Locate every Plasmodium falciparum-infected red blood cell.
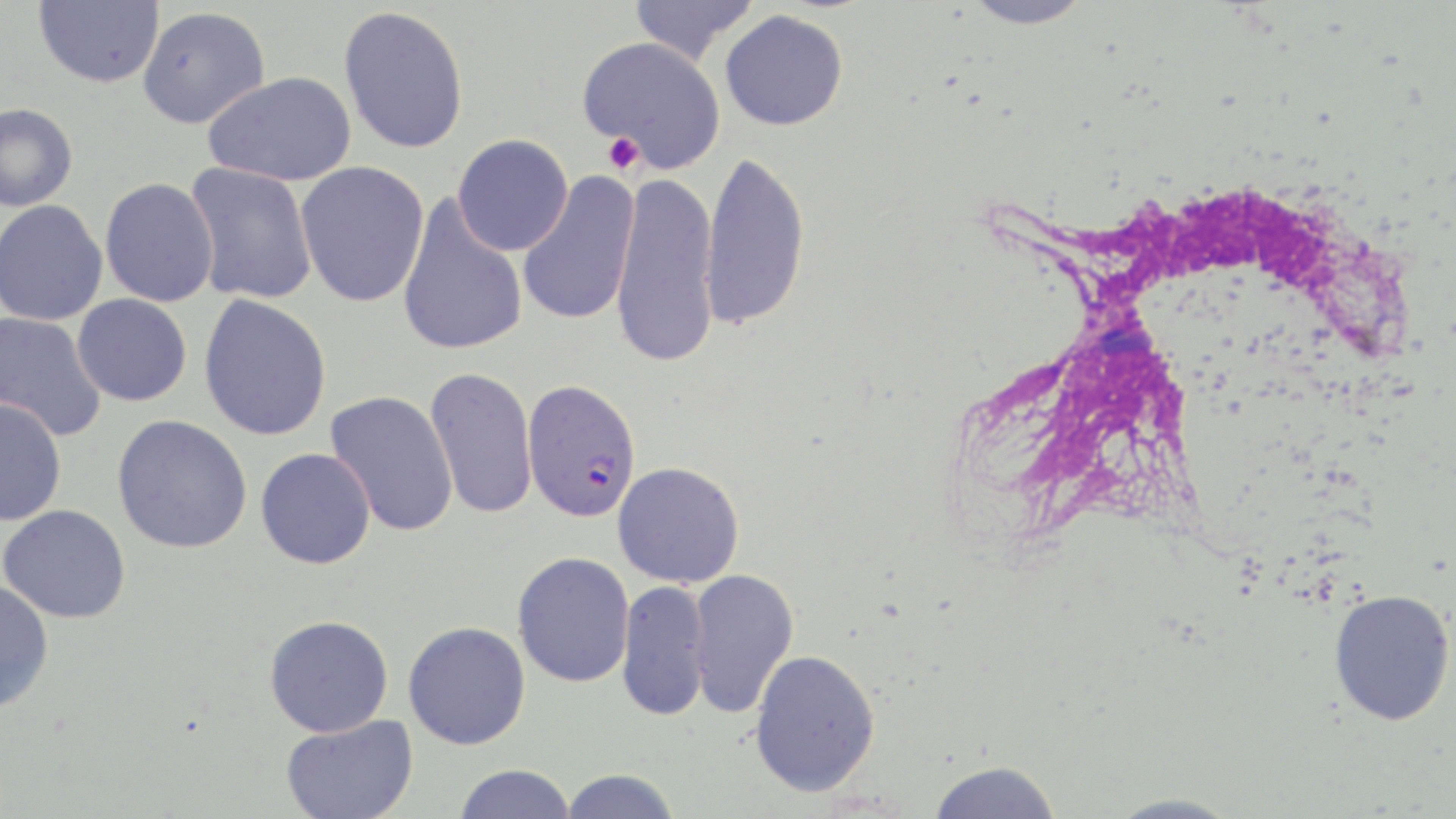
Approximate bounding boxes as (x1, y1, x2, y2) in pixels.
Plasmodium falciparum-infected red blood cells: (521, 379, 642, 523).

Uninfected red blood cell locations: (35, 0, 164, 88), (628, 0, 760, 64), (960, 0, 1094, 29), (339, 5, 469, 155), (138, 6, 270, 128), (720, 9, 849, 131), (579, 36, 725, 171), (203, 70, 357, 187), (0, 103, 78, 212), (452, 134, 573, 255), (700, 149, 810, 331), (296, 161, 429, 307), (185, 162, 318, 305), (610, 171, 721, 370), (517, 172, 641, 328), (99, 177, 218, 307), (397, 196, 528, 356), (0, 200, 108, 326), (72, 294, 192, 407), (199, 294, 332, 441), (0, 312, 107, 442), (425, 366, 538, 521), (325, 391, 459, 537), (0, 398, 67, 526), (112, 415, 253, 554), (256, 447, 376, 569), (613, 461, 745, 588), (1, 504, 131, 623), (512, 551, 634, 687), (686, 568, 799, 718), (0, 580, 54, 713), (616, 580, 711, 722), (1329, 588, 1455, 726), (264, 615, 394, 737), (403, 621, 531, 750), (748, 648, 881, 797), (281, 714, 419, 819), (928, 760, 1062, 819), (452, 763, 576, 819), (560, 769, 681, 819), (1104, 792, 1242, 819). Platelet locations: (602, 133, 645, 175). White blood cell locations: (969, 182, 1410, 543). Slide-level diagnosis: Plasmodium falciparum. Single field of view. Thin blood smear. Image is 1456×819 pixels. May-Grünwald-Giemsa-stained preparation. Light microscopy. Captured at 1000x magnification.